Comment on the morphology of the erythrocytes.
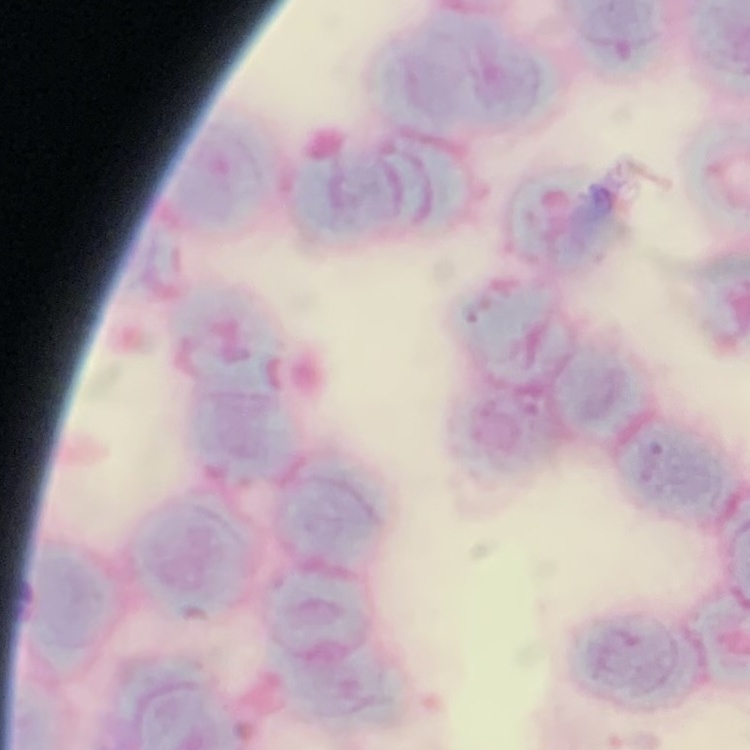
Rouleaux formation.

Stained with either Field's or Giemsa. Thin blood film. One tile cut from a larger photomicrograph.